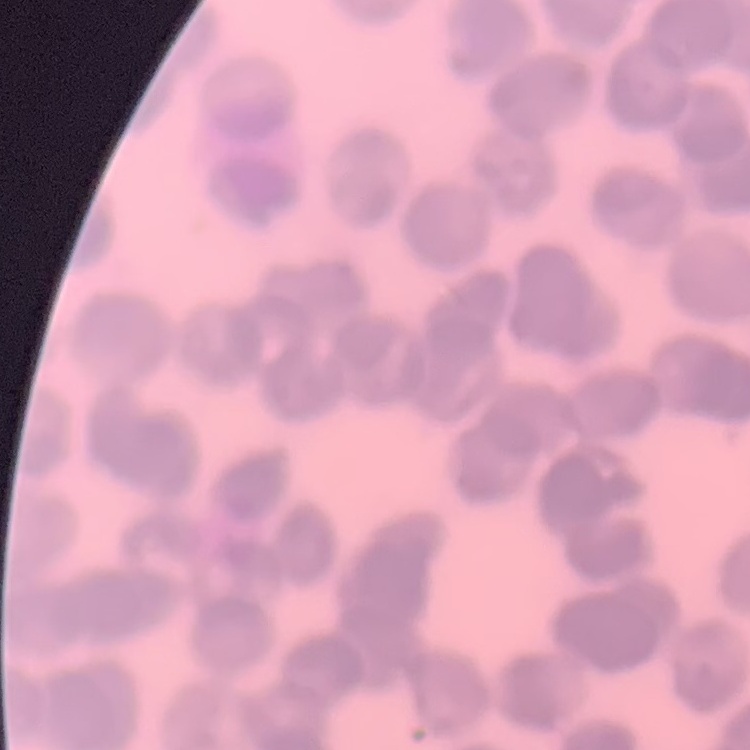
Summary:
  - Erythrocyte morphology: rouleaux formation
  - Stain: Field's or Giemsa
  - Image type: one tile cut from a larger photomicrograph
  - Preparation: thin peripheral smear